Report the malaria status of this cell.
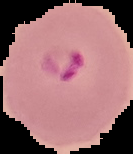
It is parasitized.

preparation = thin blood film
image size = 133×154 pixels
image type = cell region segmented out of the field of view; surrounding area masked to black